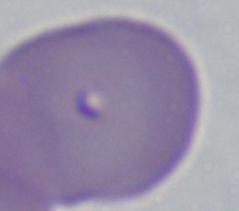

magnification = 1000x
modality = micrograph
identification = Babesia